State which cell type is depicted.
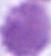

An erythrocyte.

magnification = 1000x
modality = photomicrograph